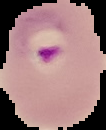
Image is 106×130 pixels. Segmented cell region on a black background. From a thin blood film. Result: Plasmodium parasites identified.